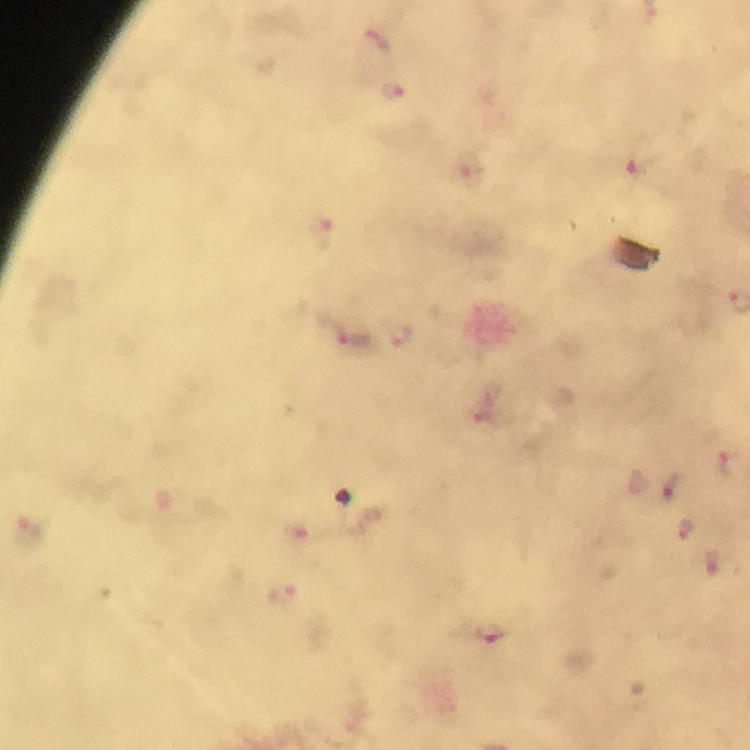
context = from a diagnostic examination for malaria
capture = smartphone mounted on the microscope
preparation = thick blood film
image size = 750×750 pixels
cropped from = one field of view
magnification = 100x
Plasmodium parasite locations = approximate centers as [x, y] in pixels: [376, 41], [395, 89], [642, 167], [322, 230], [348, 335], [401, 336], [728, 463], [672, 485], [687, 526], [715, 559], [492, 632]
stain = Giemsa
immersion oil = used